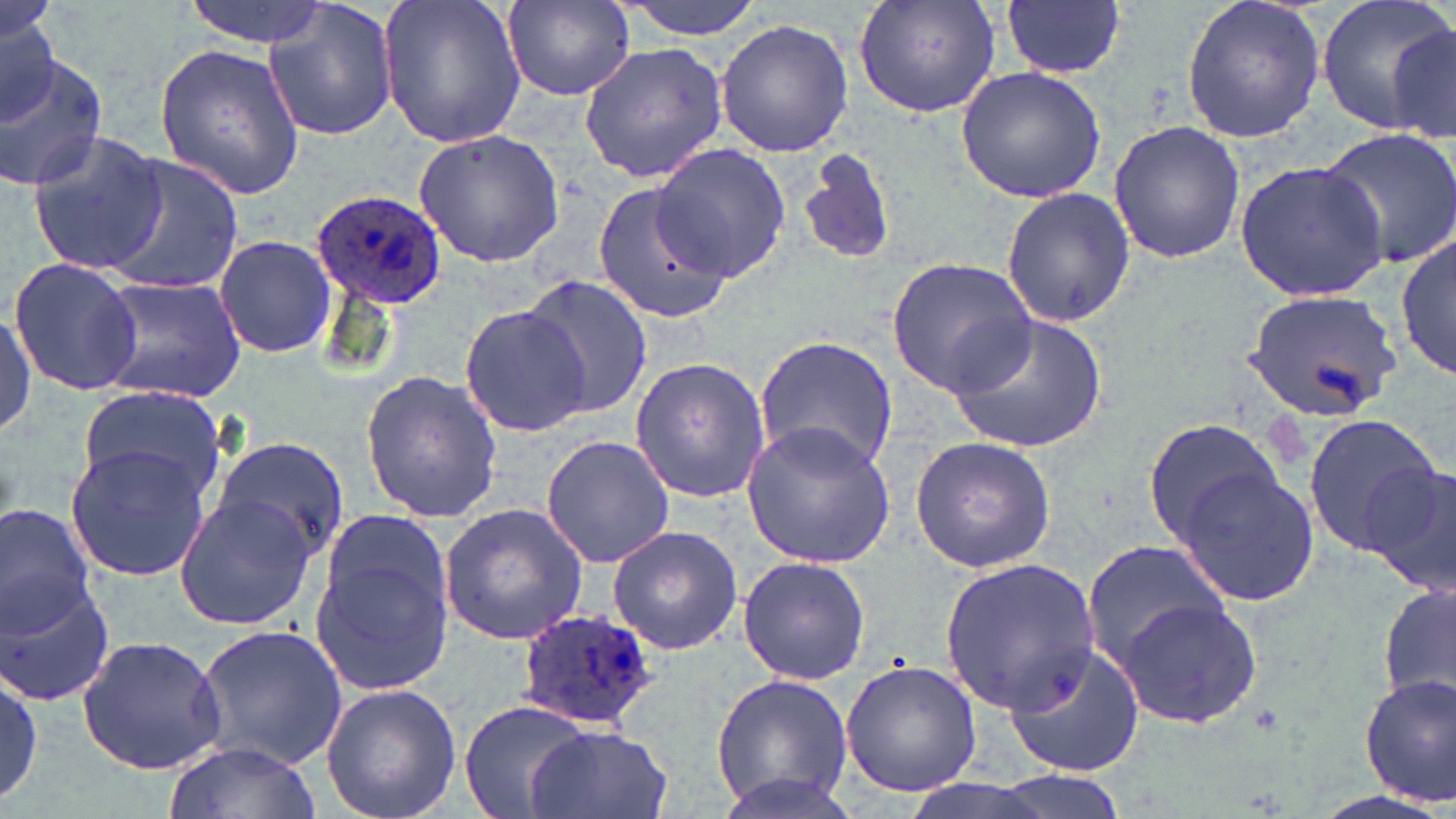

Approximate bounding boxes as named x1/y1/x2/y2 corners in pixels. Plasmodium ovale-infected red blood cell locations: (x1=309, y1=188, x2=445, y2=312), (x1=517, y1=609, x2=659, y2=728). Uninfected red blood cell locations: (x1=181, y1=0, x2=339, y2=47), (x1=376, y1=0, x2=526, y2=151), (x1=613, y1=0, x2=771, y2=38), (x1=851, y1=0, x2=1004, y2=120), (x1=1002, y1=0, x2=1125, y2=79), (x1=1179, y1=0, x2=1325, y2=145), (x1=1315, y1=0, x2=1456, y2=136), (x1=499, y1=2, x2=637, y2=100), (x1=262, y1=3, x2=400, y2=142), (x1=2, y1=19, x2=61, y2=125), (x1=715, y1=19, x2=853, y2=157), (x1=1390, y1=19, x2=1455, y2=151), (x1=153, y1=42, x2=304, y2=201), (x1=577, y1=43, x2=728, y2=183), (x1=2, y1=49, x2=108, y2=193), (x1=955, y1=65, x2=1106, y2=204), (x1=1107, y1=120, x2=1246, y2=264), (x1=1314, y1=127, x2=1456, y2=270), (x1=24, y1=129, x2=169, y2=278), (x1=411, y1=129, x2=565, y2=267), (x1=651, y1=141, x2=791, y2=282), (x1=797, y1=146, x2=898, y2=269), (x1=99, y1=155, x2=242, y2=296), (x1=1233, y1=156, x2=1393, y2=302), (x1=589, y1=182, x2=733, y2=323), (x1=999, y1=187, x2=1137, y2=327), (x1=214, y1=234, x2=336, y2=357), (x1=1396, y1=235, x2=1455, y2=382), (x1=9, y1=258, x2=144, y2=395), (x1=886, y1=259, x2=1037, y2=396), (x1=97, y1=274, x2=245, y2=402), (x1=516, y1=275, x2=654, y2=418), (x1=1242, y1=288, x2=1403, y2=422), (x1=461, y1=302, x2=591, y2=434), (x1=0, y1=307, x2=36, y2=441), (x1=946, y1=314, x2=1107, y2=453), (x1=753, y1=333, x2=901, y2=478), (x1=629, y1=356, x2=772, y2=504), (x1=358, y1=370, x2=506, y2=525), (x1=76, y1=385, x2=225, y2=497), (x1=1302, y1=413, x2=1446, y2=559), (x1=1141, y1=418, x2=1279, y2=544), (x1=740, y1=422, x2=896, y2=567), (x1=540, y1=433, x2=674, y2=569), (x1=909, y1=434, x2=1057, y2=575), (x1=211, y1=436, x2=351, y2=564), (x1=64, y1=441, x2=212, y2=582), (x1=1368, y1=461, x2=1456, y2=597), (x1=1172, y1=469, x2=1320, y2=608), (x1=173, y1=492, x2=319, y2=632), (x1=439, y1=501, x2=590, y2=645), (x1=0, y1=502, x2=101, y2=641), (x1=607, y1=525, x2=742, y2=654), (x1=309, y1=537, x2=454, y2=692), (x1=1081, y1=539, x2=1231, y2=669), (x1=737, y1=556, x2=872, y2=685), (x1=937, y1=558, x2=1101, y2=713), (x1=1, y1=574, x2=118, y2=706), (x1=1379, y1=581, x2=1456, y2=712), (x1=1117, y1=595, x2=1263, y2=730), (x1=192, y1=624, x2=348, y2=771), (x1=78, y1=635, x2=228, y2=774), (x1=1002, y1=641, x2=1145, y2=778), (x1=840, y1=661, x2=983, y2=797), (x1=0, y1=670, x2=45, y2=803), (x1=711, y1=675, x2=852, y2=809), (x1=1358, y1=675, x2=1455, y2=805), (x1=320, y1=685, x2=462, y2=819), (x1=461, y1=702, x2=594, y2=819), (x1=524, y1=722, x2=674, y2=819), (x1=162, y1=740, x2=322, y2=819), (x1=713, y1=770, x2=867, y2=819), (x1=993, y1=771, x2=1133, y2=819), (x1=885, y1=776, x2=1075, y2=819). Slide-level diagnosis: Plasmodium ovale. May-Grünwald-Giemsa-stained preparation. 1000x magnification. Light microscopy. Image is 1456×819 pixels. One field of a larger specimen. Thin blood film.